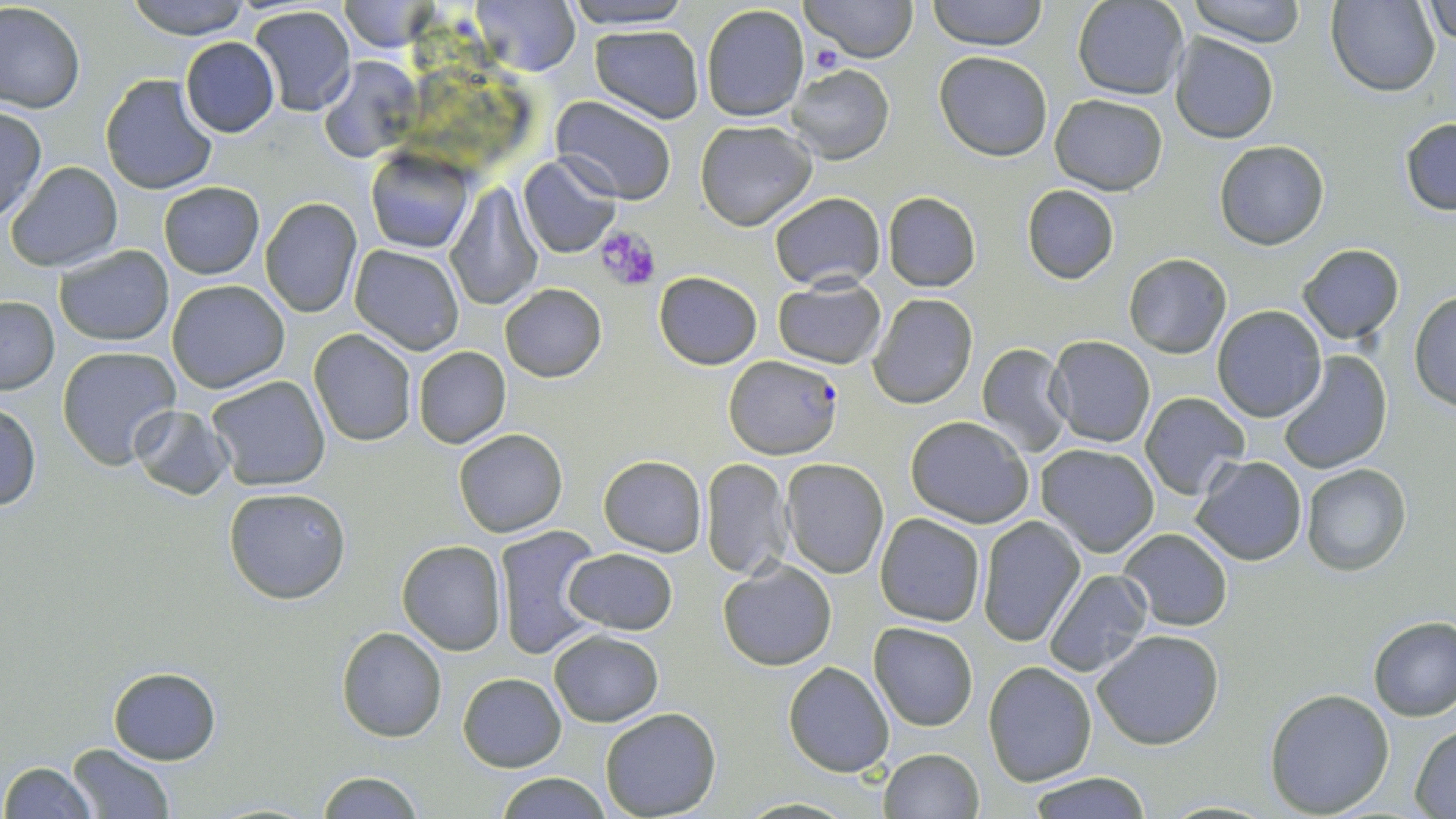
Summary:
  - Coordinate format: approximate bounding boxes as (x1, y1, x2, y2) in pixels
  - Platelet locations: (806, 42, 843, 74), (596, 226, 661, 292)
  - Uninfected red blood cell locations: (126, 0, 257, 40), (468, 0, 581, 75), (561, 0, 691, 28), (801, 0, 917, 63), (928, 0, 1046, 51), (1074, 0, 1189, 100), (1184, 0, 1310, 48), (1424, 0, 1456, 43), (337, 1, 435, 52), (1327, 1, 1440, 95), (1, 3, 85, 113), (700, 4, 811, 124), (248, 6, 357, 116), (589, 24, 705, 123), (1170, 34, 1279, 144), (181, 37, 281, 137), (934, 52, 1053, 160), (317, 56, 422, 164), (787, 64, 895, 165), (99, 74, 218, 195), (549, 94, 677, 205), (1049, 94, 1168, 194), (0, 107, 46, 222), (1401, 115, 1456, 215), (695, 120, 818, 231), (1214, 139, 1330, 250), (365, 148, 476, 253), (517, 154, 621, 258), (6, 161, 124, 272), (158, 182, 264, 279), (445, 183, 543, 312), (1021, 184, 1118, 284), (769, 190, 885, 290), (882, 192, 981, 291), (260, 197, 364, 318), (1296, 243, 1406, 346), (56, 244, 174, 346), (349, 245, 464, 354), (1125, 253, 1232, 358), (655, 272, 762, 369), (773, 276, 886, 369), (166, 279, 290, 393), (500, 284, 607, 381), (1409, 290, 1456, 411), (869, 293, 978, 409), (1, 295, 60, 393), (1211, 305, 1325, 423), (308, 329, 417, 447), (1046, 336, 1156, 448), (975, 343, 1073, 457), (58, 345, 182, 468), (412, 346, 511, 449), (1277, 350, 1393, 476), (206, 376, 331, 491), (1139, 391, 1252, 501), (0, 402, 41, 511), (127, 403, 235, 500), (904, 415, 1034, 528), (454, 428, 568, 537), (1034, 444, 1161, 558), (598, 455, 706, 557), (1192, 456, 1307, 566), (700, 457, 791, 578), (779, 458, 889, 579), (1301, 464, 1411, 576), (223, 487, 352, 605), (875, 512, 986, 627), (976, 514, 1084, 646), (494, 525, 605, 659), (1119, 528, 1233, 631), (396, 539, 507, 656), (565, 549, 678, 635), (717, 559, 836, 669), (1044, 568, 1153, 679), (1368, 617, 1456, 722), (869, 622, 978, 731), (336, 627, 449, 743), (549, 629, 662, 726), (1092, 629, 1224, 750), (983, 661, 1099, 787), (783, 662, 895, 777), (107, 667, 221, 764), (458, 672, 566, 771), (1264, 688, 1395, 817), (600, 706, 721, 818), (1412, 724, 1456, 817), (68, 743, 176, 817), (878, 748, 983, 819), (1, 761, 97, 818), (1026, 771, 1151, 818), (314, 772, 428, 818), (497, 772, 610, 819), (736, 798, 859, 817)
  - Plasmodium falciparum-infected red blood cell locations: (725, 355, 844, 457)
  - Slide-level diagnosis: Plasmodium falciparum
  - Preparation: thin blood smear
  - Stain: May-Grünwald-Giemsa
  - Image size: 1456×819 pixels
  - Field of view: single
  - Magnification: 1000x
  - Modality: light microscopy